Find the cells and give the type of each one.
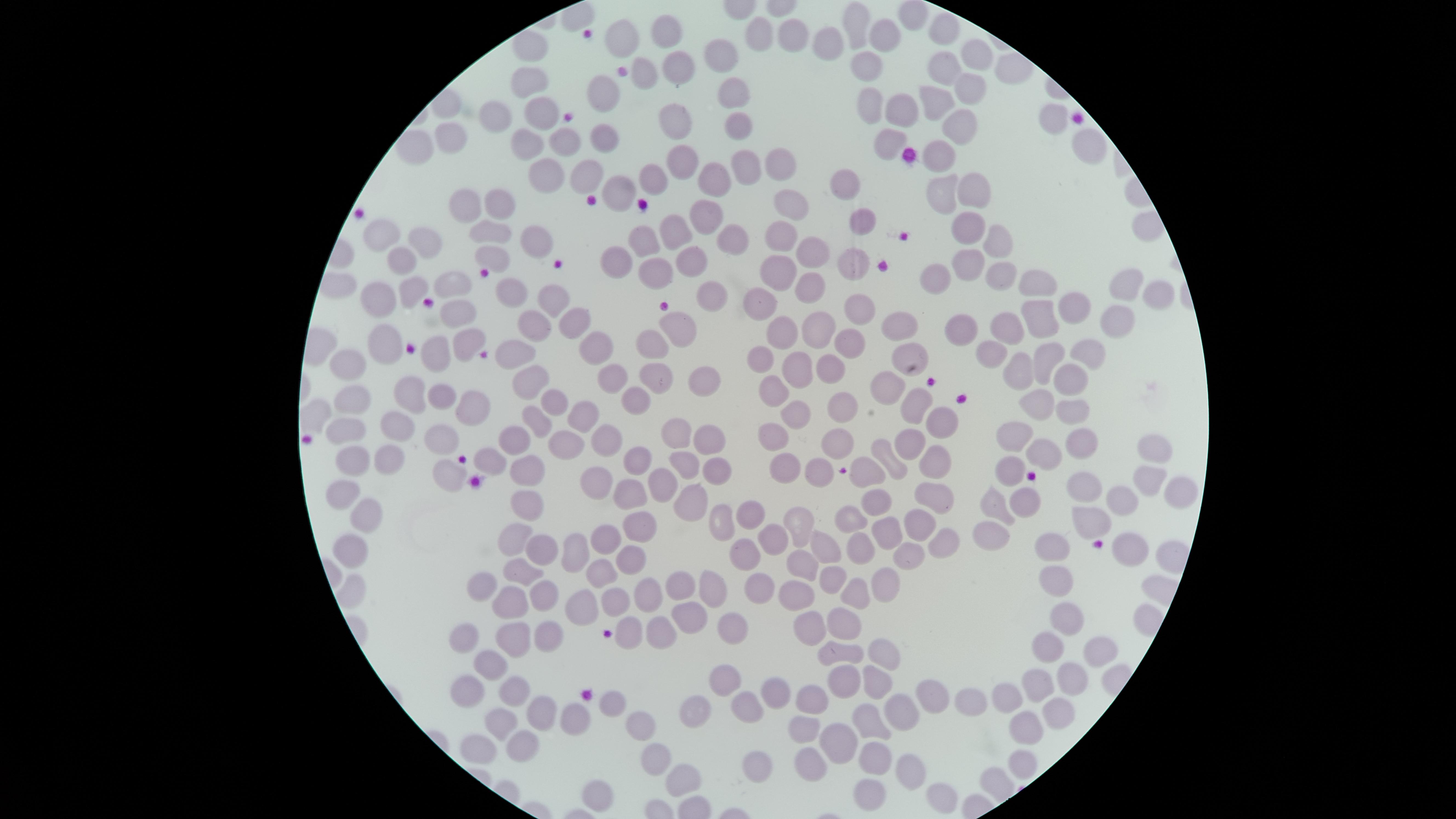

No parasitized red blood cells identified.
Approximate marker points as (x, y) in pixels.
Uninfected red blood cells: (864, 23), (665, 28), (947, 29), (627, 34), (796, 34), (760, 35), (885, 36), (824, 39), (722, 57), (973, 58), (685, 66), (865, 67), (946, 69), (643, 75), (527, 78), (604, 88), (731, 92), (962, 98), (869, 100), (936, 106), (903, 108), (540, 110), (496, 117), (673, 123), (736, 123), (953, 132), (455, 134), (603, 138), (556, 142), (887, 142), (526, 143), (940, 154), (680, 162), (744, 164), (781, 164), (587, 174), (550, 176), (710, 179), (647, 180), (841, 183), (622, 190), (971, 190), (938, 193), (788, 200), (471, 202), (501, 202), (860, 217), (710, 219), (964, 223), (680, 228), (385, 229), (495, 232), (779, 236), (537, 238), (648, 238), (735, 238), (999, 242), (429, 244), (809, 250), (690, 251), (492, 256), (399, 259), (852, 261), (971, 262), (610, 264), (656, 266), (774, 268), (1005, 274), (937, 275), (810, 280), (452, 286), (1032, 288), (1131, 289), (503, 291), (412, 292), (711, 297), (1156, 297), (377, 299), (553, 300), (761, 300), (1076, 305), (862, 306), (458, 310), (1035, 317), (682, 322), (1007, 322), (531, 323), (577, 323), (818, 324), (902, 325), (961, 325), (1112, 326), (779, 328), (385, 339), (467, 339), (594, 344), (850, 344), (656, 345), (994, 350), (908, 352), (515, 355), (762, 355), (439, 356), (1082, 357), (1053, 359), (352, 360), (1024, 365), (796, 367), (829, 367), (608, 372), (534, 374), (659, 377), (1067, 378), (704, 381), (887, 384), (413, 387), (772, 387), (442, 394), (640, 398), (348, 400), (1033, 400), (918, 401), (548, 402), (471, 407), (589, 408), (1074, 411), (842, 412), (794, 414), (535, 421), (939, 421), (399, 424), (672, 426), (344, 427), (1009, 430), (513, 434), (606, 434), (441, 436), (705, 436), (772, 439), (911, 440), (835, 441), (564, 442), (1074, 442), (1042, 450), (1159, 450), (883, 451), (350, 455), (635, 458), (386, 459), (492, 462), (531, 462), (688, 464), (941, 464), (776, 466), (718, 468), (819, 468), (1007, 468), (444, 471), (869, 471), (601, 477), (1145, 479), (661, 482), (1085, 482), (628, 490), (1179, 492), (344, 493), (930, 495), (693, 500), (876, 502), (994, 502), (1131, 502), (529, 503), (1021, 503), (755, 512), (367, 513), (725, 515), (843, 518), (793, 521), (918, 521), (1089, 521), (640, 524), (888, 531), (987, 531), (513, 532), (608, 535), (768, 539), (946, 539), (536, 545), (824, 545), (854, 545), (349, 548), (1058, 548), (574, 549), (747, 550), (1128, 550), (905, 553), (628, 562), (794, 565), (520, 567), (599, 575), (485, 581), (831, 581), (1055, 583), (758, 586), (882, 587), (356, 588), (684, 590), (712, 591), (543, 592), (856, 593), (651, 595), (799, 596), (578, 598), (613, 598), (512, 604), (692, 618), (1064, 620), (841, 624), (462, 630), (550, 630), (732, 630), (809, 633), (512, 637), (658, 637), (630, 638), (1041, 643), (878, 650), (847, 652), (1096, 654), (490, 666), (1067, 676), (873, 679), (1039, 680), (721, 682), (846, 683), (470, 689), (932, 690), (520, 692), (973, 693), (772, 694), (1012, 694), (815, 699), (608, 704), (745, 709), (701, 710), (905, 712), (1056, 715), (877, 718), (539, 719), (641, 719), (501, 721), (574, 722), (809, 724), (1024, 730), (834, 744), (520, 745), (471, 750), (809, 757), (656, 759), (877, 762), (1018, 762), (753, 764), (912, 770), (682, 780), (867, 791), (597, 794), (938, 797).
No white blood cells identified.

Summary:
  - Capture: smartphone photograph through the microscope eyepiece
  - Image size: 1456×819 pixels
  - Field of view: single
  - Visible region: circular
  - Stain: Giemsa
  - Preparation: thin blood film